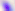

magnification: 400x
identification: Toxoplasma gondii
modality: micrograph